Locate and identify every blood parasite.
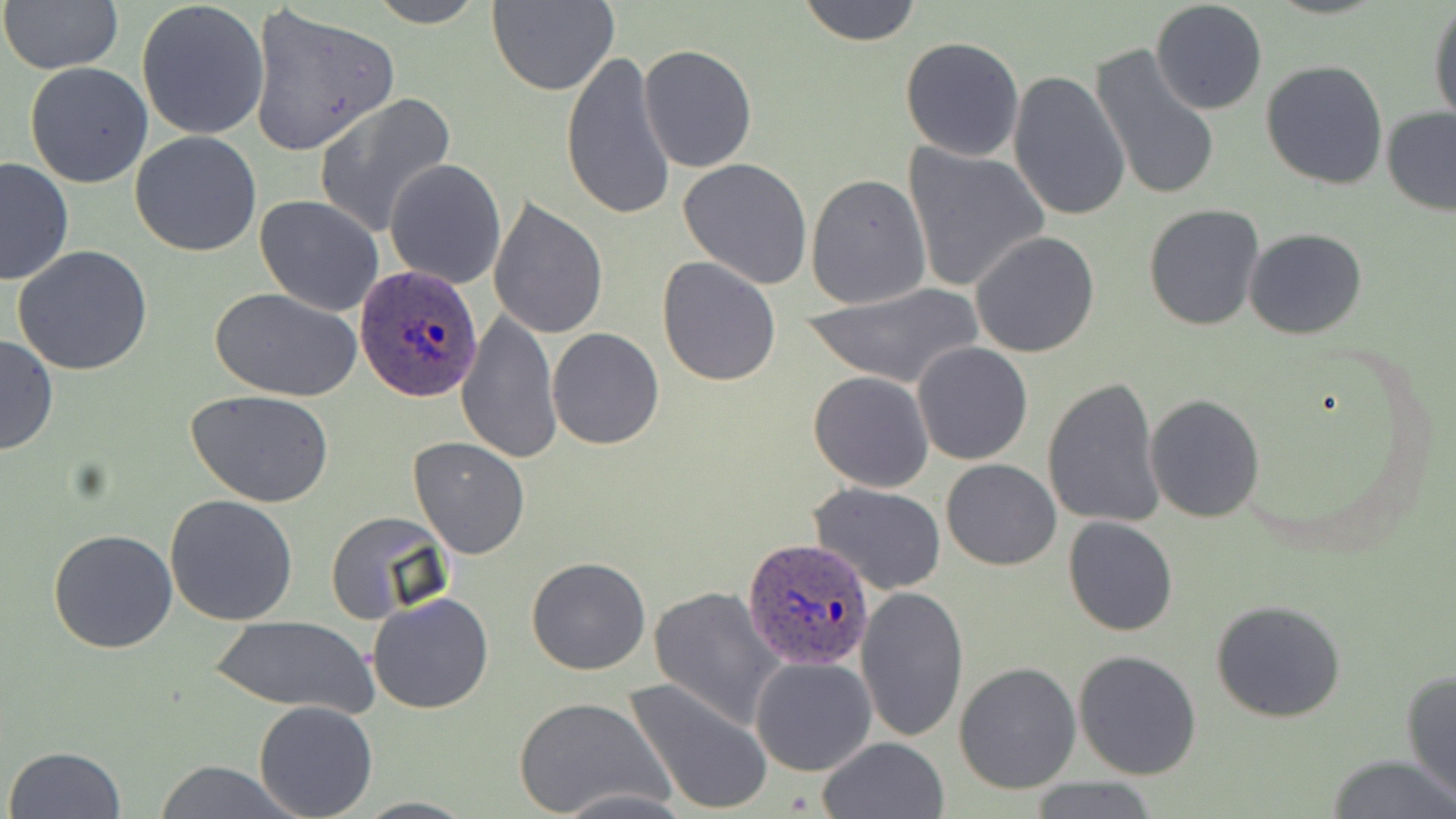
Approximate bounding boxes as (x1, y1, x2, y2) in pixels.
Plasmodium ovale-infected red blood cells: (354, 264, 483, 400), (743, 539, 877, 670).
No Plasmodium falciparum, Plasmodium malariae, Plasmodium vivax, Babesia divergens, or Trypanosoma brucei observed.

slide_level_diagnosis: Plasmodium ovale
field_of_view: one of a larger specimen
uninfected_red_blood_cell_locations: 'approximate bounding boxes as (x1, y1, x2, y2) in pixels: (2, 0, 125, 76), (362, 0, 491, 27), (486, 0, 619, 95), (1150, 0, 1268, 116), (136, 1, 271, 141), (795, 1, 924, 46), (1428, 3, 1456, 125), (247, 4, 402, 156), (900, 36, 1025, 162), (638, 44, 757, 172), (1089, 44, 1222, 204), (561, 49, 677, 222), (1260, 59, 1387, 190), (24, 62, 154, 188), (1007, 69, 1131, 224), (313, 93, 456, 238), (1381, 107, 1456, 216), (129, 130, 261, 257), (902, 145, 1050, 294), (0, 156, 76, 287), (679, 157, 814, 288), (384, 158, 507, 289), (805, 173, 930, 310), (255, 195, 384, 316), (488, 198, 607, 340), (1143, 203, 1266, 331), (1244, 229, 1367, 339), (970, 231, 1100, 358), (12, 245, 153, 376), (657, 257, 783, 388), (803, 284, 984, 388), (210, 287, 363, 401), (455, 308, 562, 465), (547, 328, 665, 449), (0, 334, 58, 457), (912, 342, 1034, 465), (807, 370, 934, 492), (1041, 376, 1165, 530), (186, 389, 337, 509), (1144, 393, 1266, 523), (406, 436, 530, 558), (940, 458, 1061, 571), (808, 480, 947, 595), (165, 494, 298, 626), (324, 509, 454, 625), (50, 516, 295, 642), (1063, 516, 1179, 637), (47, 528, 178, 653), (526, 557, 651, 675), (649, 585, 786, 728), (855, 587, 968, 743), (367, 592, 494, 714), (1210, 599, 1348, 722), (210, 615, 378, 715), (1074, 649, 1202, 778), (750, 655, 876, 775), (953, 662, 1081, 795), (1400, 665, 1456, 805), (621, 675, 774, 815), (511, 694, 669, 815), (253, 700, 378, 819), (818, 737, 949, 819), (6, 745, 127, 818), (1328, 755, 1456, 818), (150, 760, 302, 818), (1021, 779, 1165, 817), (550, 787, 691, 817), (352, 796, 477, 817)'
preparation: thin blood smear
stain: May-Grünwald-Giemsa
modality: optical microscopy
magnification: 1000x
image_size: 1456×819 pixels